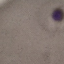
Result: malaria parasites identified. Photographed with a smartphone camera at the microscope eyepiece. Thin blood smear. Cell patch, automatically extracted from a larger field of view and resized to 64 × 64 pixels. Giemsa-stained preparation.